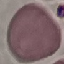
Summary:
  - Malaria status: uninfected
  - Stain: Giemsa
  - Capture: smartphone through the microscope eyepiece
  - Preparation: thin blood smear
  - Image type: cell patch, automatically extracted from a larger field of view and resized to 64 × 64 pixels